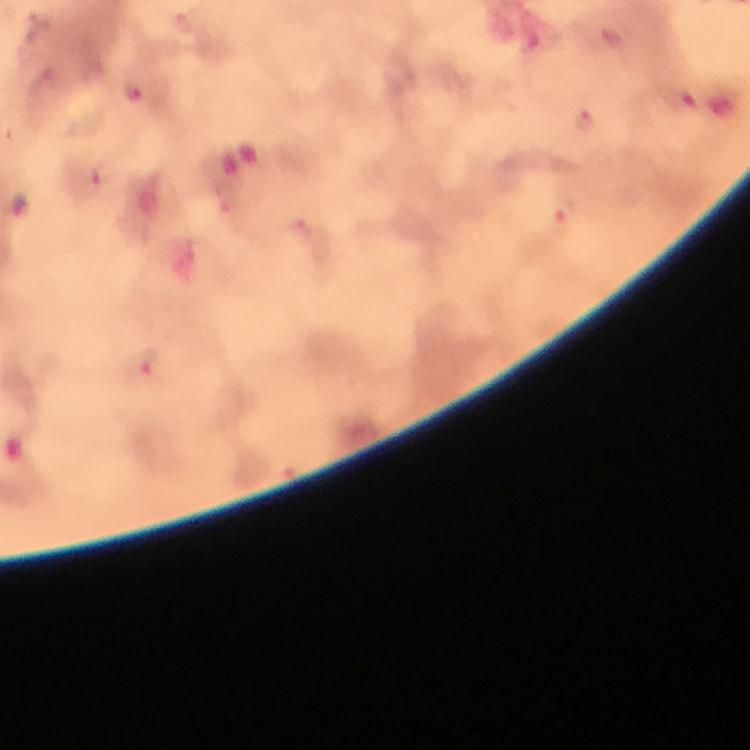

cropped_from: a single field of view
stain: Giemsa
capture: smartphone camera through the microscope
magnification: 100x
immersion_oil: applied
context: from a diagnostic examination for malaria
image_size: 750×750 pixels
preparation: thick smear
malaria_parasite_locations: 'approximate centers as [x, y] in pixels: [38, 24], [132, 94], [582, 116], [103, 176], [17, 204], [565, 217], [145, 368]'